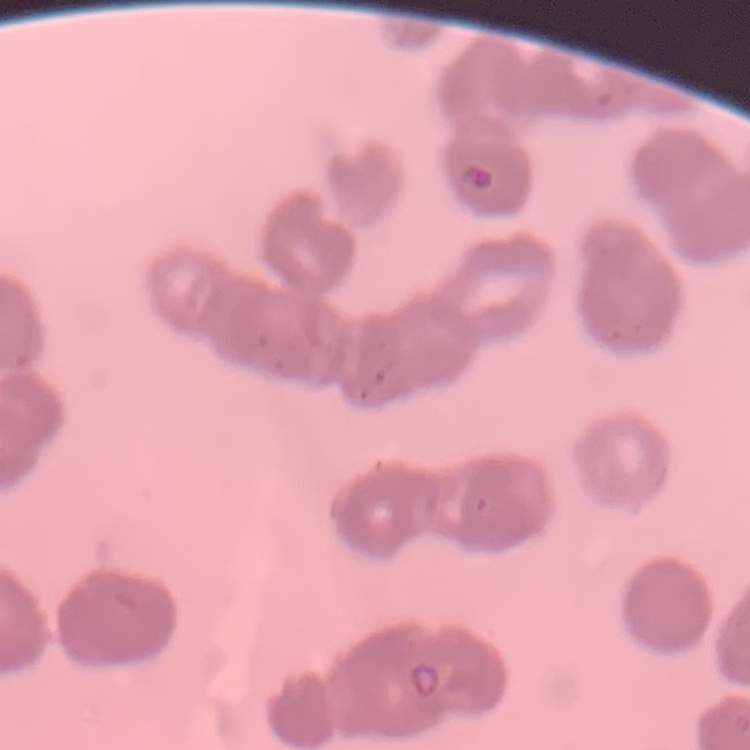

red_blood_cell_morphology: rouleaux formation
preparation: thin peripheral smear
image_type: square crop of a larger photomicrograph
stain: Field's or Giemsa